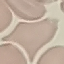 Result: no malaria parasites detected. Thin blood smear. Giemsa stain. Photographed with a smartphone camera at the microscope eyepiece. Automatically extracted cell patch, resized to 64 × 64 pixels.